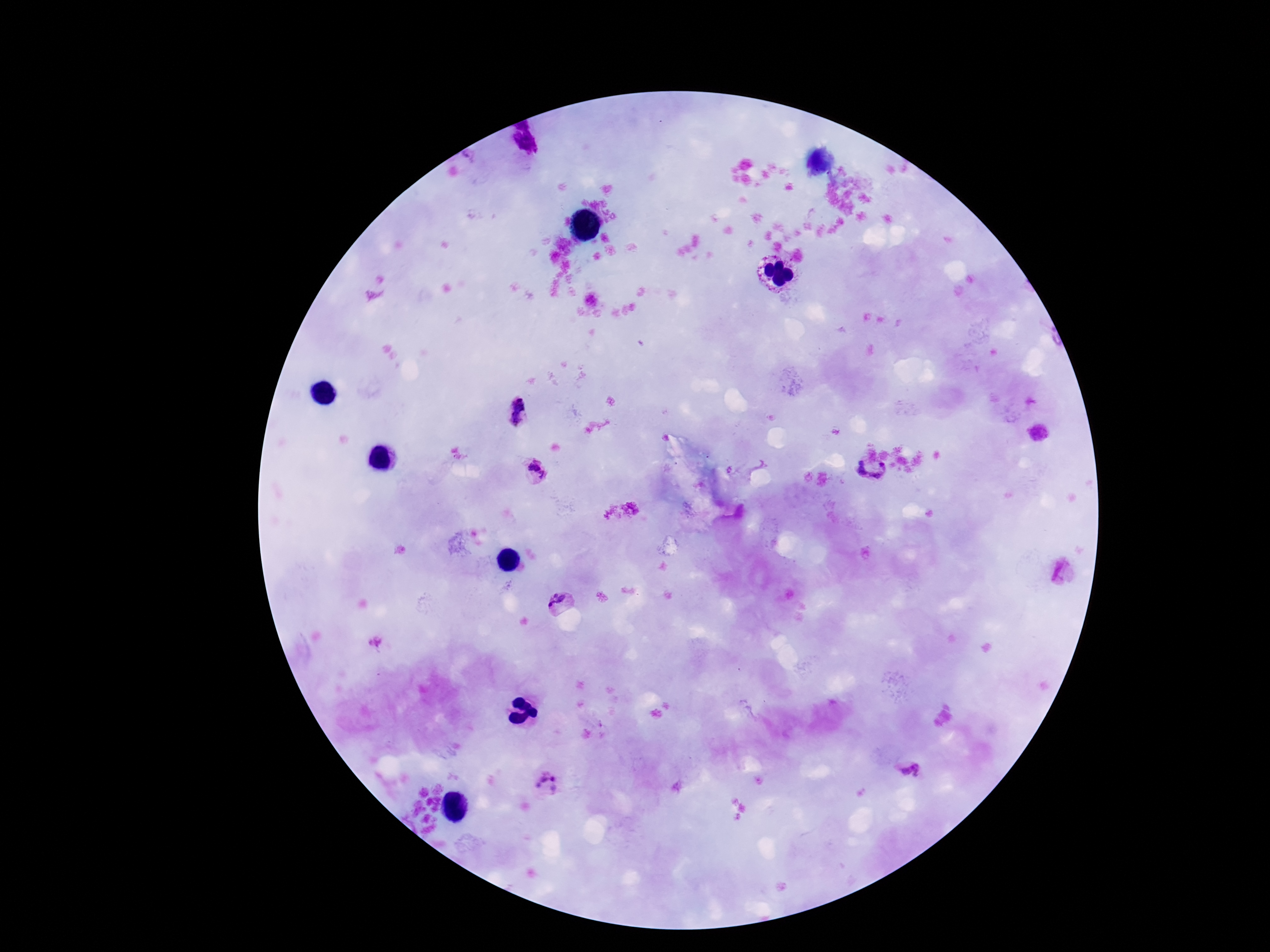 Approximate centers as {x, y} in pixels. Plasmodium parasite locations: {516, 413}, {871, 470}, {539, 474}, {559, 605}, {909, 772}, {544, 785}. Thick peripheral-blood smear. Image is 1270×952 pixels. Patient malaria status: positive. Giemsa stain. Smartphone photograph taken through the microscope eyepiece. 100x magnification. Single field of view.